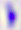

modality = micrograph
identification = Toxoplasma gondii
magnification = 400x